Comment on the morphology of the red blood cells.
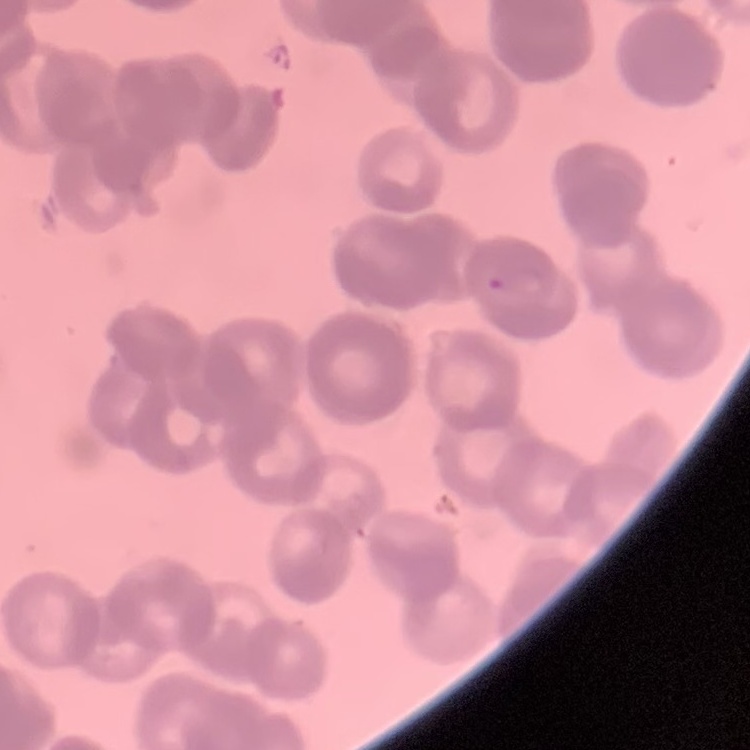

Rouleaux formation.

Field's or Giemsa stain. Thin peripheral smear. One tile cut from a larger photomicrograph.